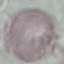
malaria_status: uninfected
image_type: cell patch, automatically extracted from a larger field of view and resized to 64 × 64 pixels
preparation: thin smear
stain: Giemsa
capture: smartphone camera at the microscope eyepiece